Report the malaria status of this cell.
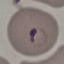

It is parasitized.

Summary:
  - Image type: automatically extracted cell patch, resized to 64 × 64 pixels
  - Stain: Giemsa
  - Capture: smartphone camera at the microscope eyepiece
  - Preparation: thin smear